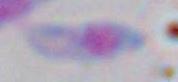

magnification = 1000x
identification = Toxoplasma gondii
modality = photomicrograph